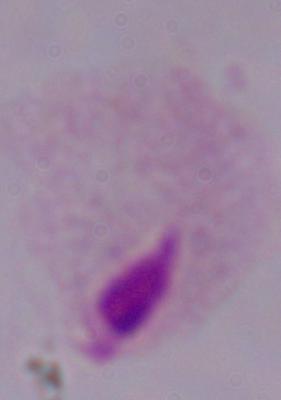
A trichomonad is shown. Captured at 1000x magnification. Micrograph.